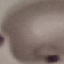
result: malaria parasites identified
image_type: automatically extracted cell patch, resized to 64 × 64 pixels
stain: Giemsa
preparation: thin smear
capture: smartphone through the microscope eyepiece